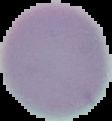

From a thin blood film. The area outside the segmented cell region is set to black. Malaria status: uninfected. Image is 112×121 pixels.